Name the cell type shown.
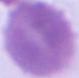

An erythrocyte.

Summary:
  - Modality: photomicrograph
  - Magnification: 1000x